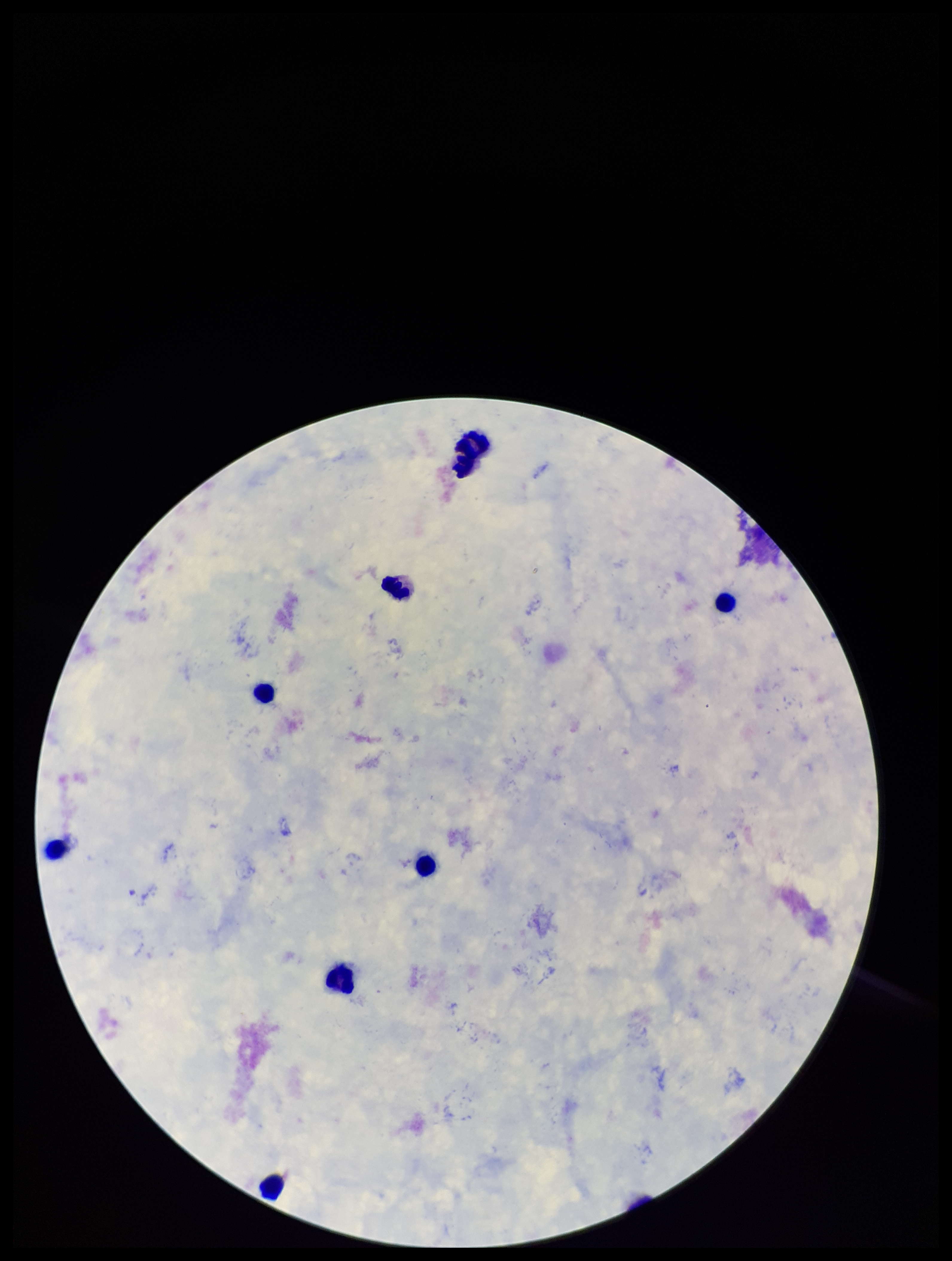
preparation: thick smear
patient_malaria_status: negative
capture: smartphone photograph through the microscope eyepiece
plasmodium_parasites: none detected
field_of_view: single
leukocyte_count: 8
parasite_count: 0
image_size: 952×1261 pixels
stain: Giemsa